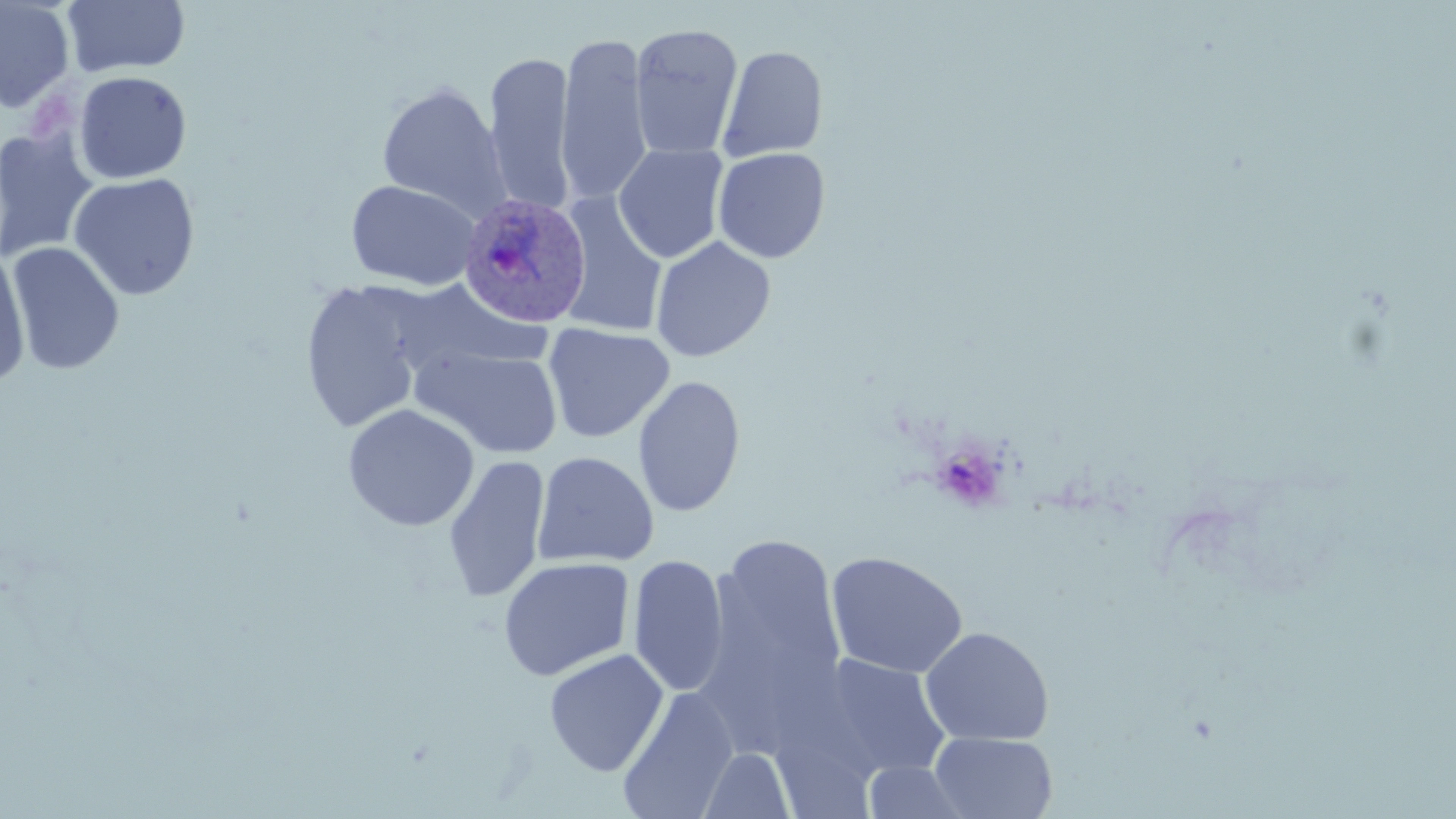

Summary:
  - Coordinate format: approximate bounding boxes as [x1, y1, x2, y2] in pixels
  - Plasmodium ovale-infected red blood cell locations: [452, 192, 592, 323]
  - Platelet locations: [932, 442, 1009, 512]
  - Uninfected red blood cell locations: [0, 0, 76, 112], [62, 0, 191, 78], [629, 23, 743, 160], [555, 33, 654, 206], [718, 45, 828, 162], [483, 49, 576, 215], [73, 71, 192, 184], [376, 81, 510, 219], [1, 126, 100, 263], [613, 144, 729, 264], [712, 147, 830, 264], [68, 172, 201, 301], [345, 179, 481, 291], [555, 193, 668, 337], [650, 236, 775, 362], [5, 241, 125, 376], [0, 243, 32, 387], [392, 279, 550, 377], [299, 280, 433, 434], [542, 323, 675, 443], [409, 343, 564, 459], [632, 374, 746, 518], [343, 403, 480, 532], [533, 451, 659, 568], [443, 454, 550, 603], [701, 531, 847, 731], [826, 551, 969, 679], [628, 554, 730, 698], [498, 556, 634, 681], [919, 626, 1054, 746], [544, 648, 669, 777], [816, 654, 951, 781], [617, 687, 738, 819], [929, 732, 1058, 818], [698, 747, 796, 818], [861, 760, 975, 818]
  - Slide-level diagnosis: Plasmodium ovale
  - Preparation: thin blood smear
  - Field of view: single
  - Stain: May-Grünwald-Giemsa
  - Modality: optical microscopy
  - Image size: 1456×819 pixels
  - Magnification: 1000x